Report the malaria status.
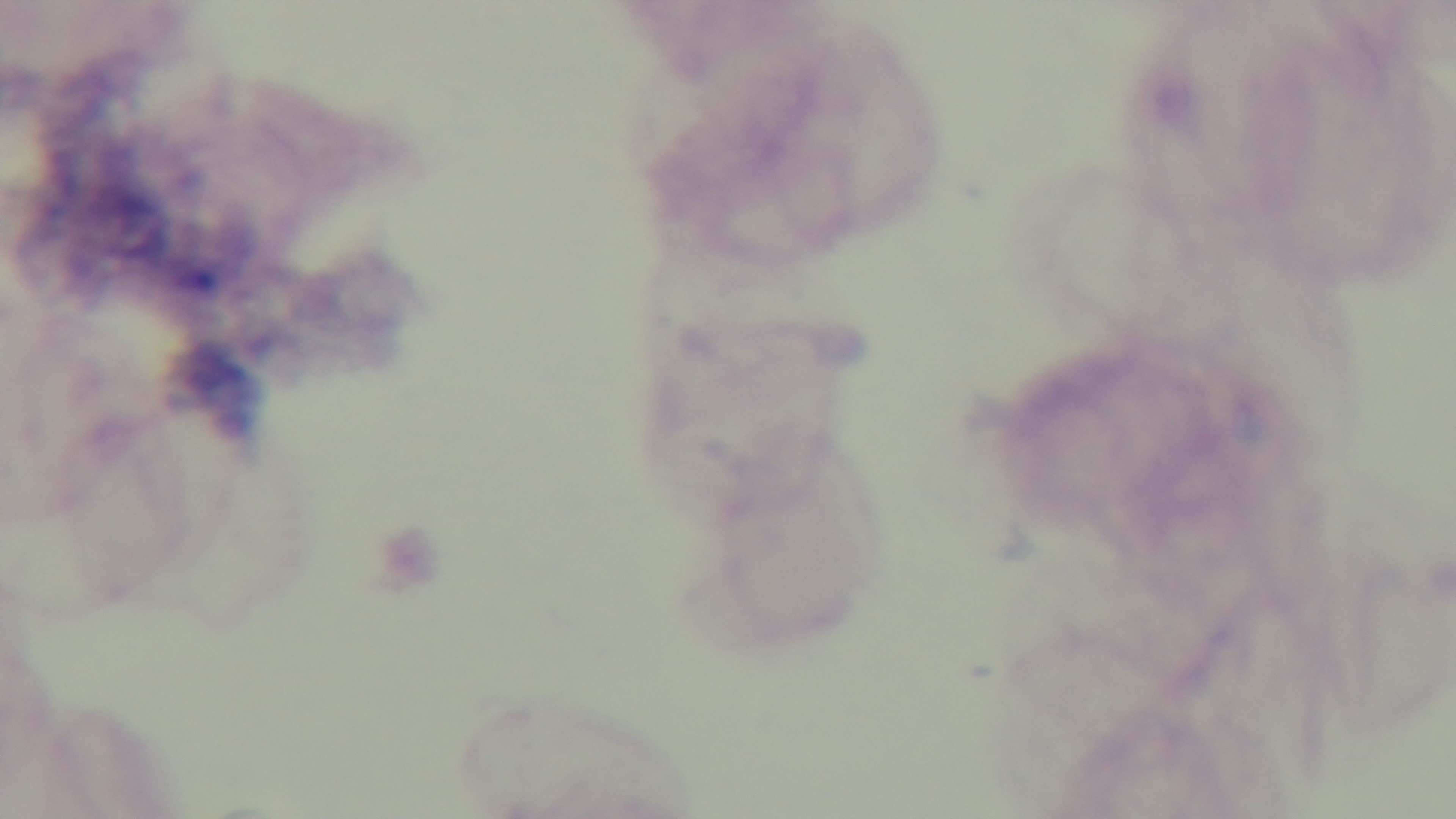
It is uninfected.

Giemsa stain. Captured with a mounted 4K digital camera. 100x oil-immersion objective. Light microscopy. Preparation: thick smear. Single field of view.